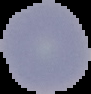

From a thin blood film. Malaria status: uninfected. The area outside the segmented cell region is set to black. Image is 91×94 pixels.